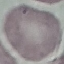
Malaria status: uninfected. Thin blood smear. Automatically extracted cell patch, resized to 64 × 64 pixels. Acquired by smartphone through the microscope eyepiece. Giemsa stain.